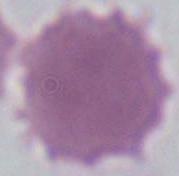

Summary:
  - Identification: red blood cell
  - Magnification: 1000x
  - Modality: micrograph